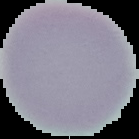
Summary:
  - Image type: segmented cell region with the area outside set to black
  - Malaria status: uninfected
  - Preparation: thin blood film
  - Image size: 139×139 pixels